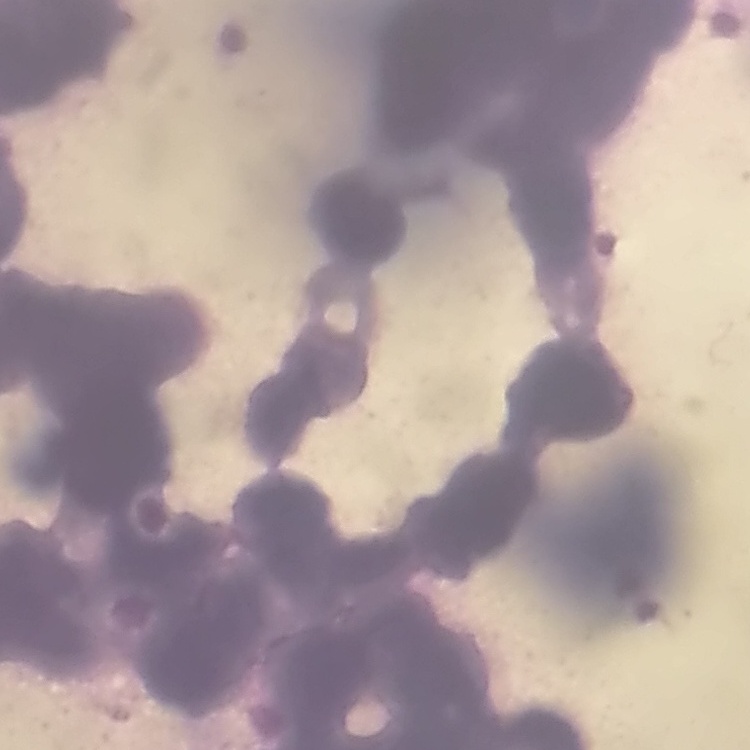
The erythrocytes show rouleaux formation. One tile cut from a larger photomicrograph. Field's or Giemsa stain. Thin blood film.